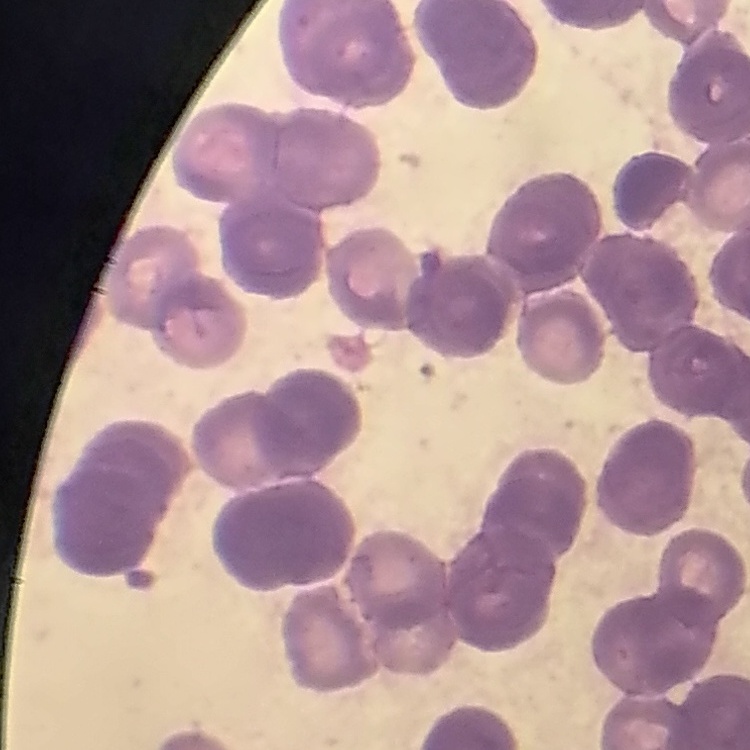
The red blood cells exhibit rouleaux formation. Stained with either Field's or Giemsa. Thin peripheral smear. Square crop of a larger photomicrograph.